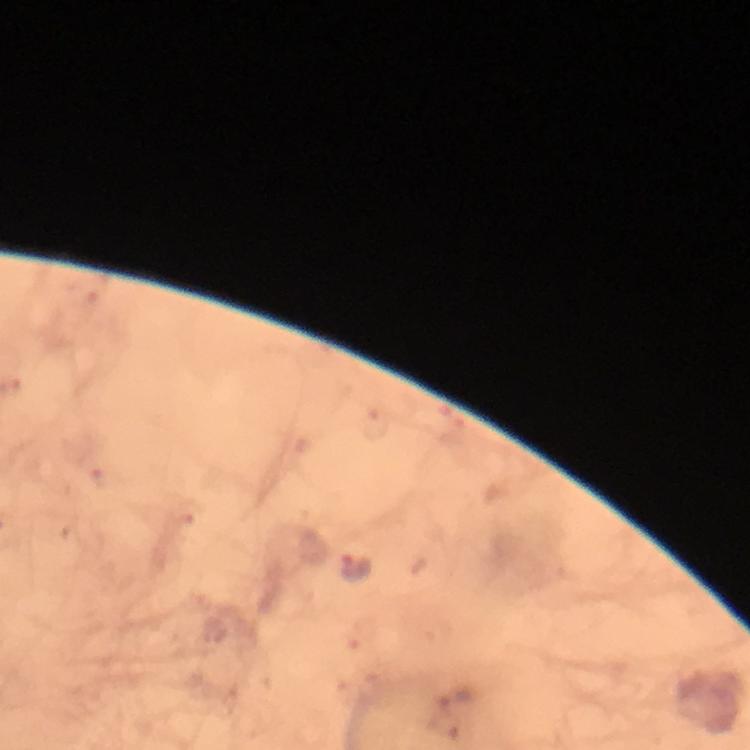

stain = Giemsa
immersion oil = applied
image size = 750×750 pixels
cropped from = one field of view
magnification = 100x
context = from a diagnostic examination for malaria
preparation = thick smear
Plasmodium parasite locations = approximate centers as [x, y] in pixels: [356, 568]
capture = smartphone photograph through a microscope